Assess this cell for malaria.
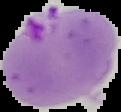

It is parasitized.

image type = cell region segmented out of the field of view; surrounding area masked to black
preparation = thin blood film
image size = 121×112 pixels